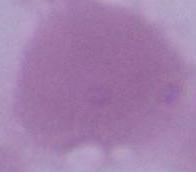 Captured at 1000x magnification. An erythrocyte is seen. Micrograph.